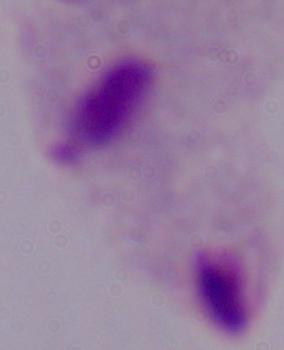
Summary:
  - Magnification: 1000x
  - Identification: trichomonad
  - Modality: micrograph